Comment on the background quality.
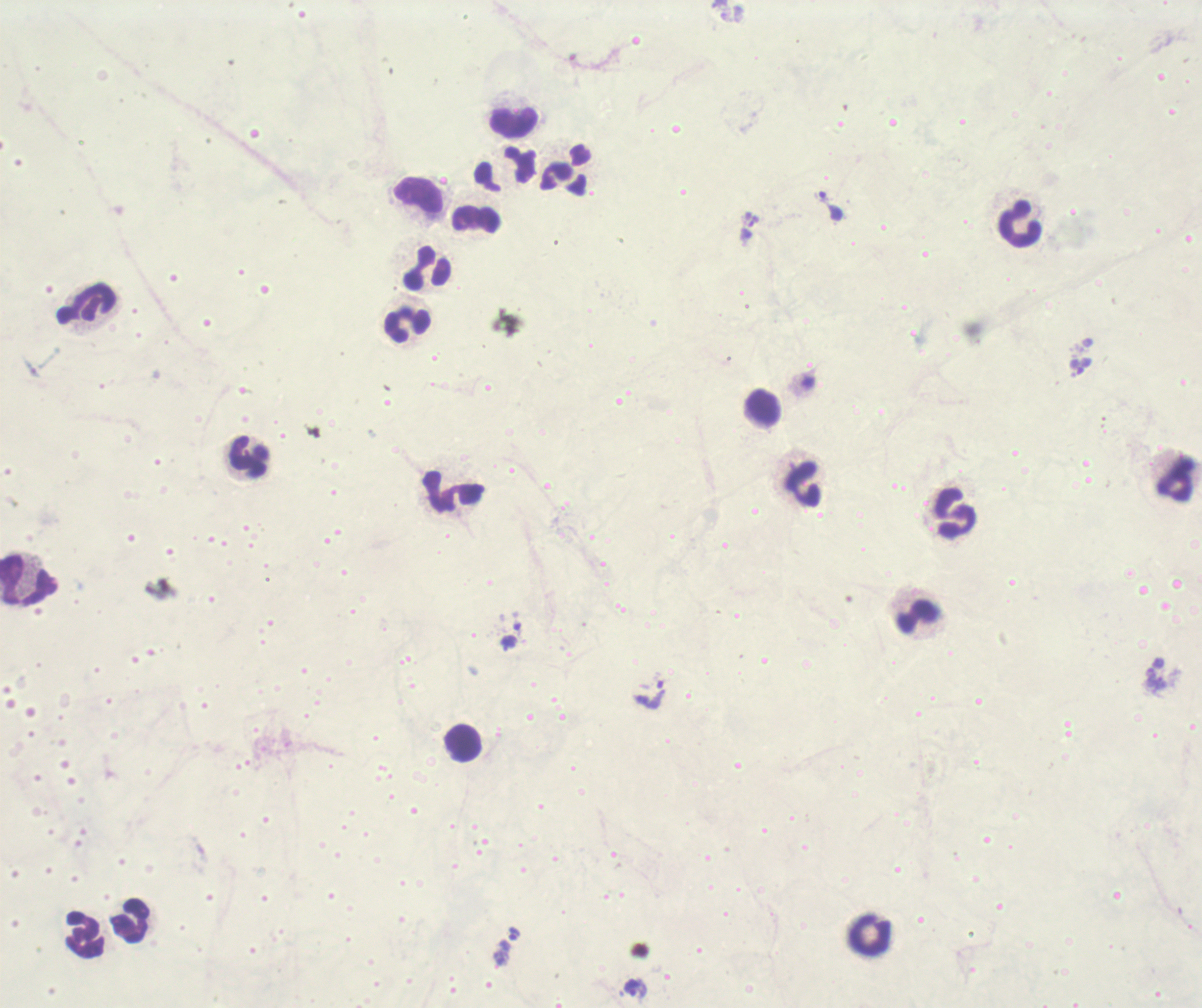
It is poor.

Approximate centers as (x, y) in pixels.
Summary:
  - Leukocyte locations: (513, 121), (505, 170), (565, 171), (419, 198), (476, 219), (1020, 223), (426, 267), (87, 305), (407, 324), (763, 409), (249, 458), (1175, 478), (801, 483), (454, 491), (954, 513), (29, 580), (917, 617), (462, 744), (131, 921), (85, 934), (870, 934)
  - Trophozoite locations: (749, 225), (514, 933), (636, 988)
  - Stain: Romanowsky
  - Magnification: 100x
  - Field of view: single
  - Result: malaria parasites detected
  - Context: previously used in an actual diagnosis
  - Preparation: thick blood smear
  - Coloration quality: bad
  - Image size: 1202×1008 pixels